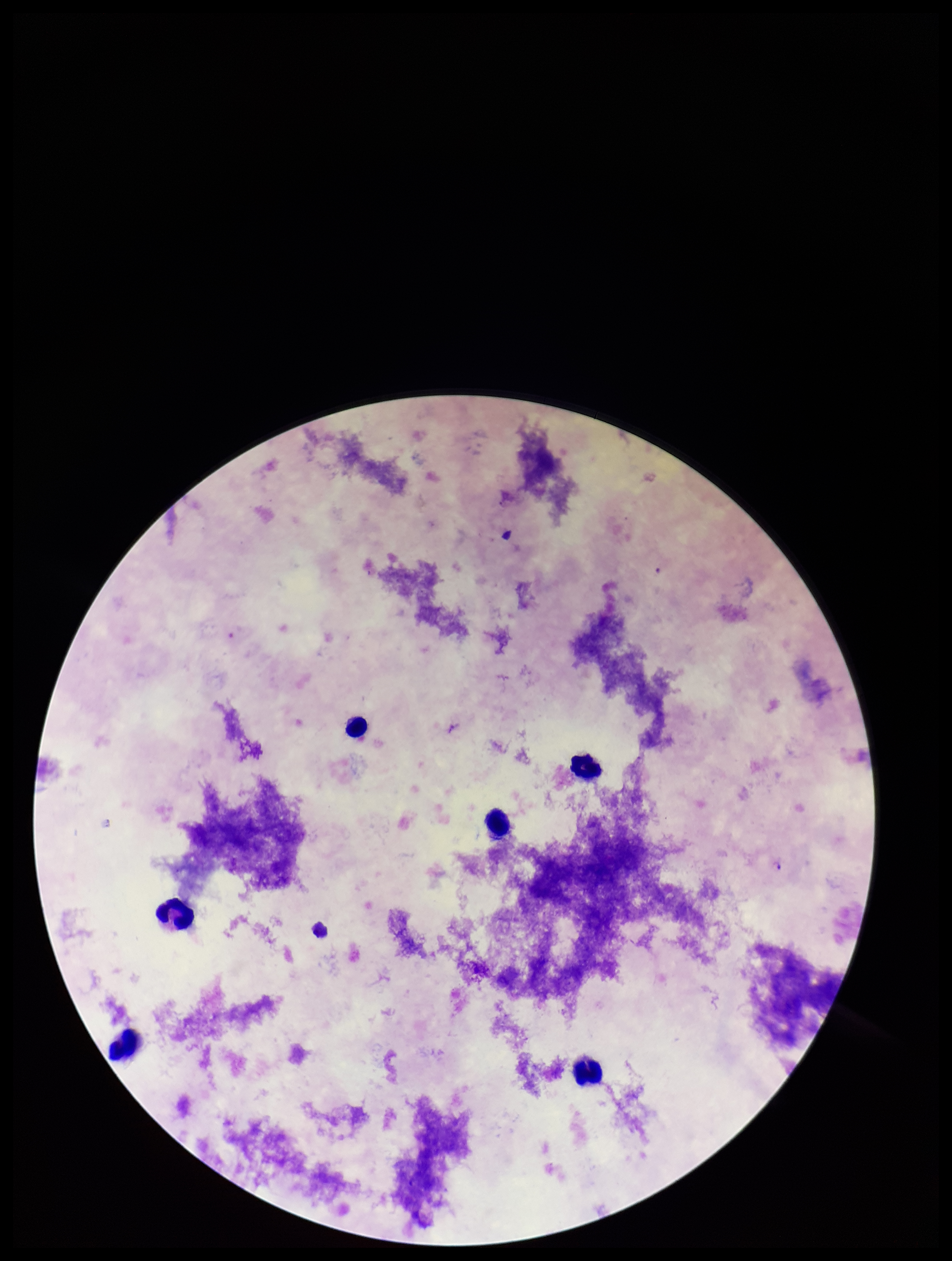
Summary:
  - Stain: Giemsa
  - Image size: 952×1261 pixels
  - Patient malaria status: positive
  - Field of view: single
  - Parasite count: 3
  - Leukocyte count: 6
  - Capture: smartphone photograph through the microscope eyepiece
  - Preparation: thick
  - Species reported for this patient: Plasmodium falciparum
  - Plasmodium parasites: detected